State which parasite is depicted.
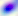
This is Toxoplasma gondii.

Summary:
  - Magnification: 400x
  - Modality: photomicrograph